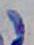

Summary:
  - Modality: photomicrograph
  - Identification: Toxoplasma gondii
  - Magnification: 1000x